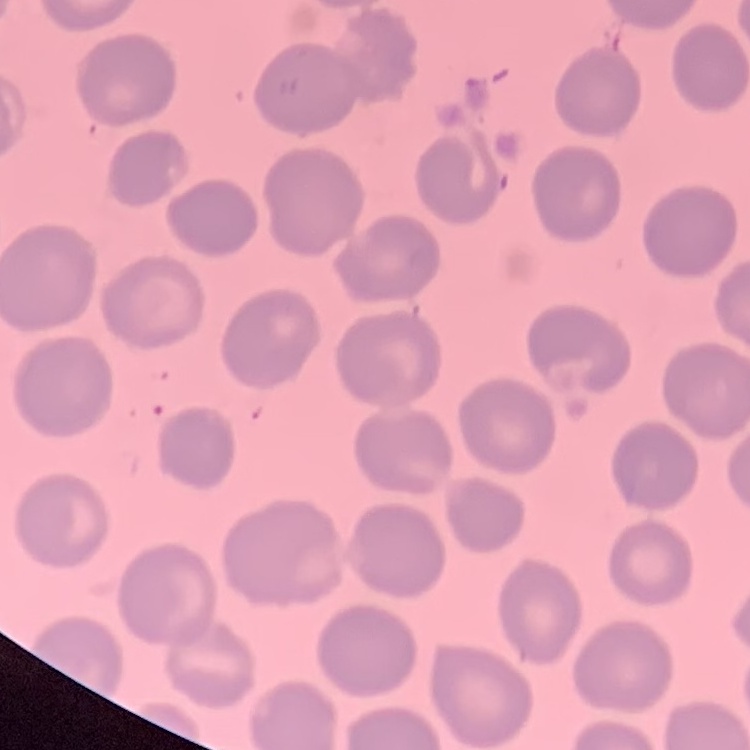
{
  "erythrocyte_morphology": "no rouleaux formation",
  "stain": "Field's or Giemsa",
  "image_type": "one tile cut from a larger photomicrograph",
  "preparation": "thin blood film"
}